Comment on the morphology of the erythrocytes.
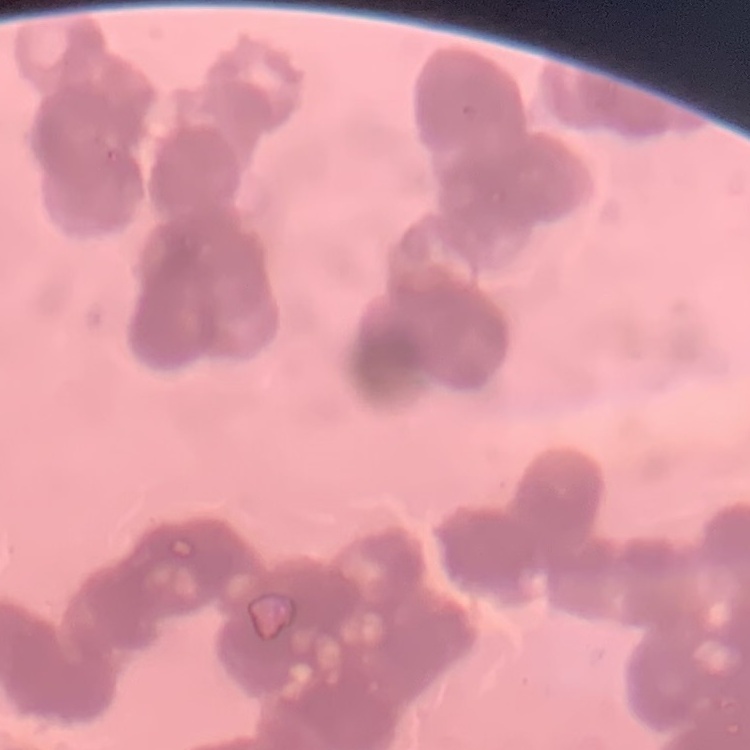

They show rouleaux formation.

Summary:
  - Stain: Field's or Giemsa
  - Preparation: thin peripheral smear
  - Image type: one tile cut from a larger photomicrograph